Assess this cell for malaria.
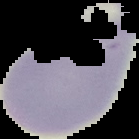

It is uninfected.

Summary:
  - Image size: 139×139 pixels
  - Image type: segmented cell region with the area outside set to black
  - Preparation: thin blood film